Report the malaria status of this cell.
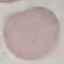
Uninfected.

Summary:
  - Capture: smartphone through the microscope eyepiece
  - Image type: cell patch, automatically extracted from a larger field of view and resized to 64 × 64 pixels
  - Stain: Giemsa
  - Preparation: thin blood smear